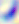
Summary:
  - Identification: Toxoplasma gondii
  - Modality: photomicrograph
  - Magnification: 400x